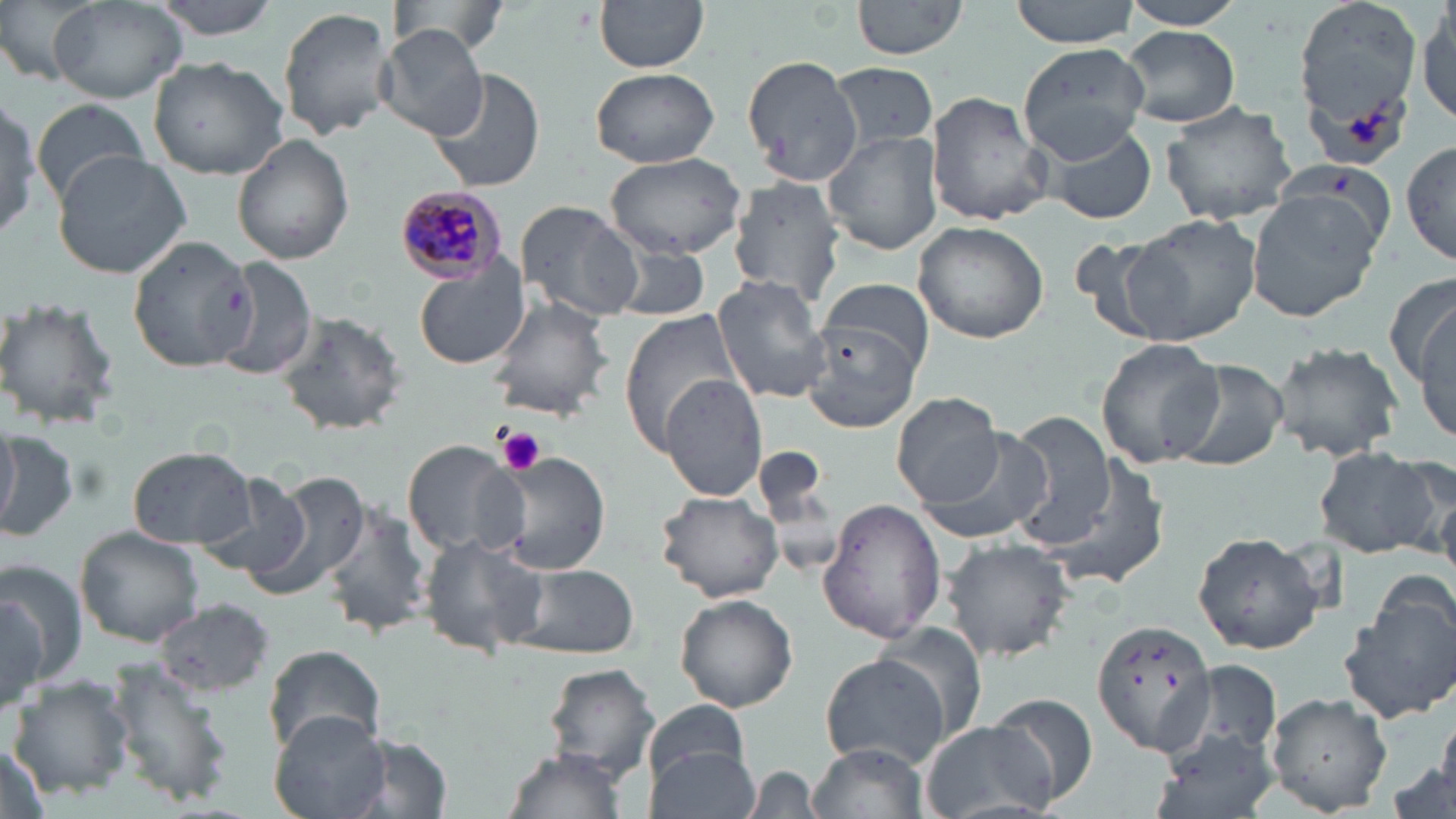

Summary:
  - Coordinate format: approximate bounding boxes as (x1, y1, x2, y2) in pixels
  - Plasmodium malariae-infected red blood cell locations: (390, 183, 507, 287)
  - Platelet locations: (497, 426, 546, 475)
  - Uninfected red blood cell locations: (44, 0, 190, 104), (148, 0, 283, 39), (385, 0, 507, 57), (595, 0, 708, 72), (852, 0, 974, 61), (1012, 0, 1140, 48), (1119, 0, 1251, 30), (1294, 0, 1424, 156), (1414, 4, 1454, 127), (277, 6, 396, 141), (375, 24, 487, 140), (1122, 25, 1242, 128), (1008, 42, 1153, 173), (740, 55, 863, 186), (146, 56, 288, 178), (831, 61, 940, 156), (425, 65, 546, 193), (590, 68, 719, 168), (924, 91, 1051, 224), (0, 94, 51, 239), (1160, 99, 1302, 228), (31, 102, 153, 205), (1037, 121, 1162, 227), (824, 130, 943, 257), (232, 135, 354, 264), (1400, 138, 1455, 269), (52, 148, 192, 279), (605, 152, 749, 256), (728, 178, 846, 306), (1245, 192, 1382, 321), (515, 200, 644, 321), (1124, 213, 1262, 342), (913, 220, 1049, 343), (129, 234, 258, 371), (610, 242, 711, 321), (210, 256, 318, 380), (413, 261, 530, 371), (1385, 269, 1456, 402), (712, 274, 833, 403), (820, 277, 935, 377), (1408, 294, 1455, 448), (487, 296, 614, 422), (0, 297, 121, 432), (620, 309, 743, 455), (275, 312, 408, 435), (802, 319, 920, 434), (1094, 338, 1221, 468), (1270, 342, 1403, 463), (1164, 357, 1291, 470), (659, 374, 766, 500), (891, 393, 1007, 508), (1007, 410, 1116, 547), (0, 415, 19, 531), (920, 427, 1055, 544), (1, 430, 78, 546), (404, 440, 524, 560), (1313, 444, 1440, 557), (130, 445, 258, 547), (484, 452, 611, 575), (1387, 453, 1456, 570), (1043, 458, 1170, 595), (235, 467, 373, 606), (197, 471, 314, 582), (657, 488, 783, 602), (817, 498, 947, 645), (325, 501, 437, 643), (74, 526, 205, 648), (1193, 531, 1324, 654), (419, 533, 548, 659), (942, 538, 1075, 662), (1, 559, 86, 691), (508, 562, 640, 661), (1342, 577, 1456, 725), (0, 590, 49, 716), (675, 595, 798, 712), (154, 599, 276, 696), (1092, 616, 1216, 757), (877, 623, 987, 742), (263, 643, 386, 760), (818, 653, 953, 771), (105, 659, 232, 809), (1178, 659, 1283, 762), (544, 663, 660, 783), (8, 677, 132, 797), (1266, 692, 1395, 815), (987, 694, 1099, 809), (645, 698, 748, 790), (269, 710, 393, 819), (1439, 710, 1456, 798), (921, 720, 1060, 819), (352, 732, 454, 819), (1148, 732, 1281, 819), (809, 742, 928, 819), (644, 745, 761, 818), (504, 747, 632, 815)
  - Slide-level diagnosis: Plasmodium malariae
  - Stain: May-Grünwald-Giemsa
  - Preparation: thin blood film
  - Image size: 1456×819 pixels
  - Field of view: one of a larger specimen
  - Modality: light microscopy
  - Magnification: 1000x